Report the malaria status of this cell.
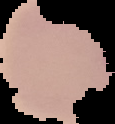
Parasitized.

Summary:
  - Image size: 115×124 pixels
  - Image type: segmented cell region with the area outside set to black
  - Preparation: thin blood smear